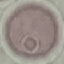
Result: no malaria parasites detected. Giemsa-stained preparation. Automatically extracted cell patch, resized to 64 × 64 pixels. Thin blood film. Acquired by smartphone through the microscope eyepiece.